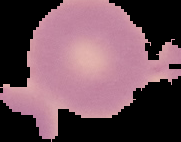
Malaria status: uninfected. Segmented cell region on a black background. From a thin blood smear. Image is 181×142 pixels.